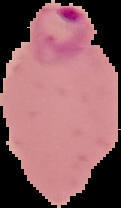

{
  "preparation": "thin blood film",
  "malaria_status": "parasitized",
  "image_size": "121×208 pixels",
  "image_type": "segmented cell region with the area outside set to black"
}